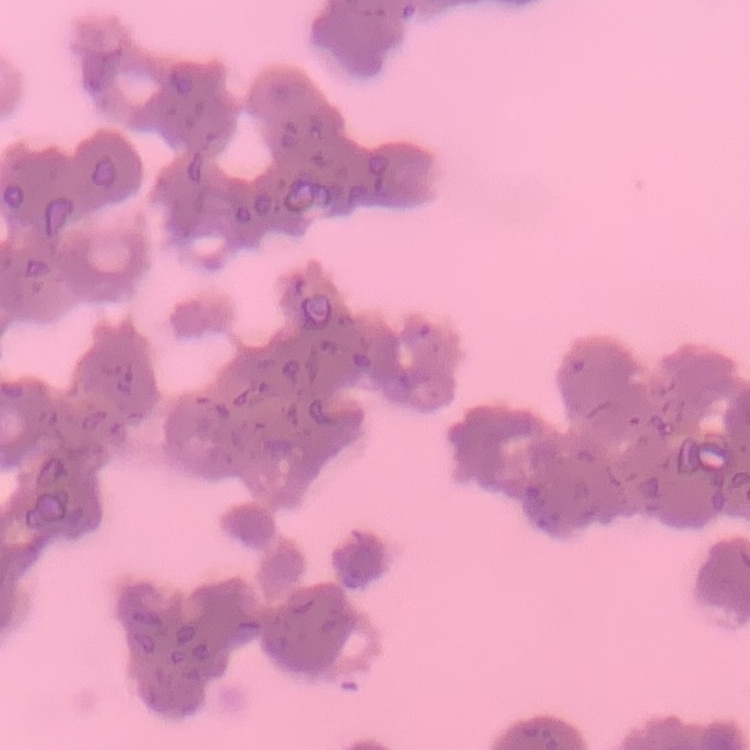
Summary:
  - Red blood cell morphology: rouleaux formation
  - Image type: square crop of a larger photomicrograph
  - Stain: Field's or Giemsa
  - Preparation: thin blood smear